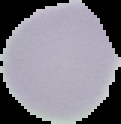
Image is 121×124 pixels. Segmented cell region on a black background. From a thin blood film. Malaria status: uninfected.